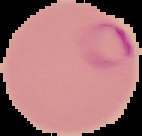

image_size: 142×136 pixels
result: Plasmodium parasites detected
image_type: segmented cell region on a black background
preparation: thin blood smear